Point out each Plasmodium parasite.
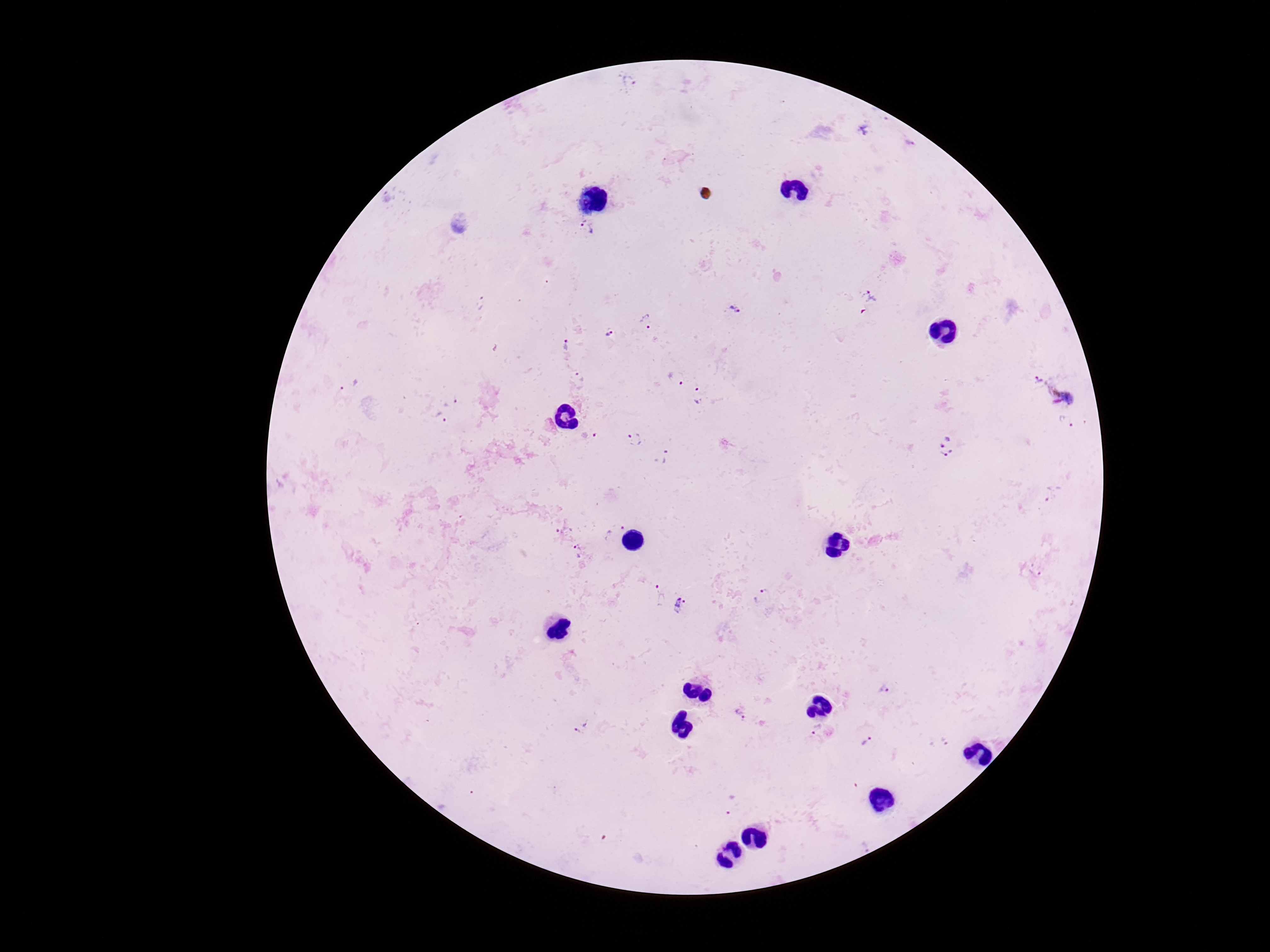

Approximate object centers, in pixels from the top-left corner.
Plasmodium parasites: (x=630, y=84), (x=907, y=144), (x=588, y=228), (x=871, y=298), (x=733, y=309), (x=647, y=321), (x=609, y=336), (x=566, y=344), (x=579, y=377), (x=675, y=378), (x=1039, y=378), (x=349, y=384), (x=699, y=395), (x=1070, y=397), (x=451, y=399), (x=439, y=419), (x=1067, y=422), (x=589, y=436), (x=634, y=440), (x=945, y=446), (x=664, y=458), (x=1053, y=494), (x=564, y=530), (x=614, y=530), (x=580, y=552), (x=1037, y=570), (x=656, y=596), (x=763, y=597), (x=678, y=605), (x=885, y=690), (x=740, y=714), (x=586, y=724), (x=814, y=729), (x=578, y=731), (x=867, y=741), (x=943, y=742), (x=732, y=804).

Summary:
  - Stain: Giemsa
  - Field of view: one from this slide
  - Magnification: 100x
  - Capture: smartphone camera through the microscope eyepiece
  - Image size: 1270×952 pixels
  - Patient malaria status: infected
  - Preparation: thick blood smear